Locate every malaria parasite.
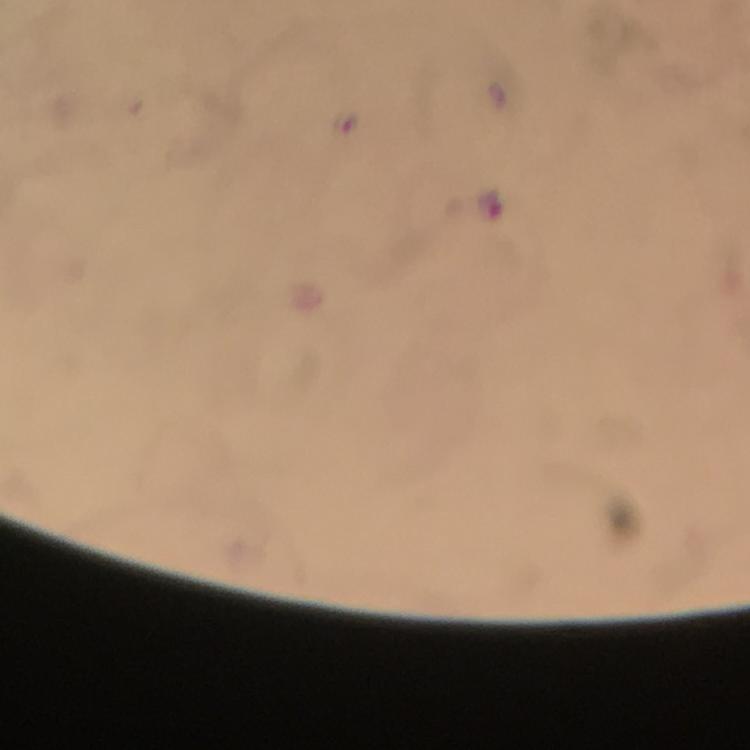
Approximate centers as {x, y} in pixels.
Malaria parasites: {488, 204}.

capture = smartphone camera through the microscope
context = from a malaria diagnostic workup
preparation = thick blood film
magnification = 100x
immersion oil = applied
image size = 750×750 pixels
cropped from = a single field of view
stain = Giemsa